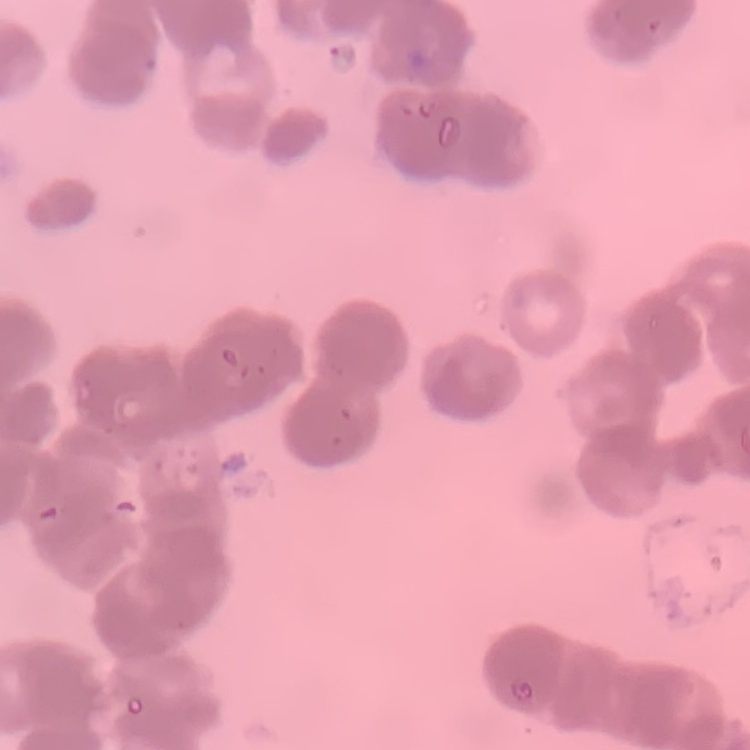
Summary:
  - Red blood cell morphology: rouleaux formation
  - Image type: one tile cut from a larger photomicrograph
  - Stain: Field's or Giemsa
  - Preparation: thin peripheral smear